Locate and identify every blood parasite.
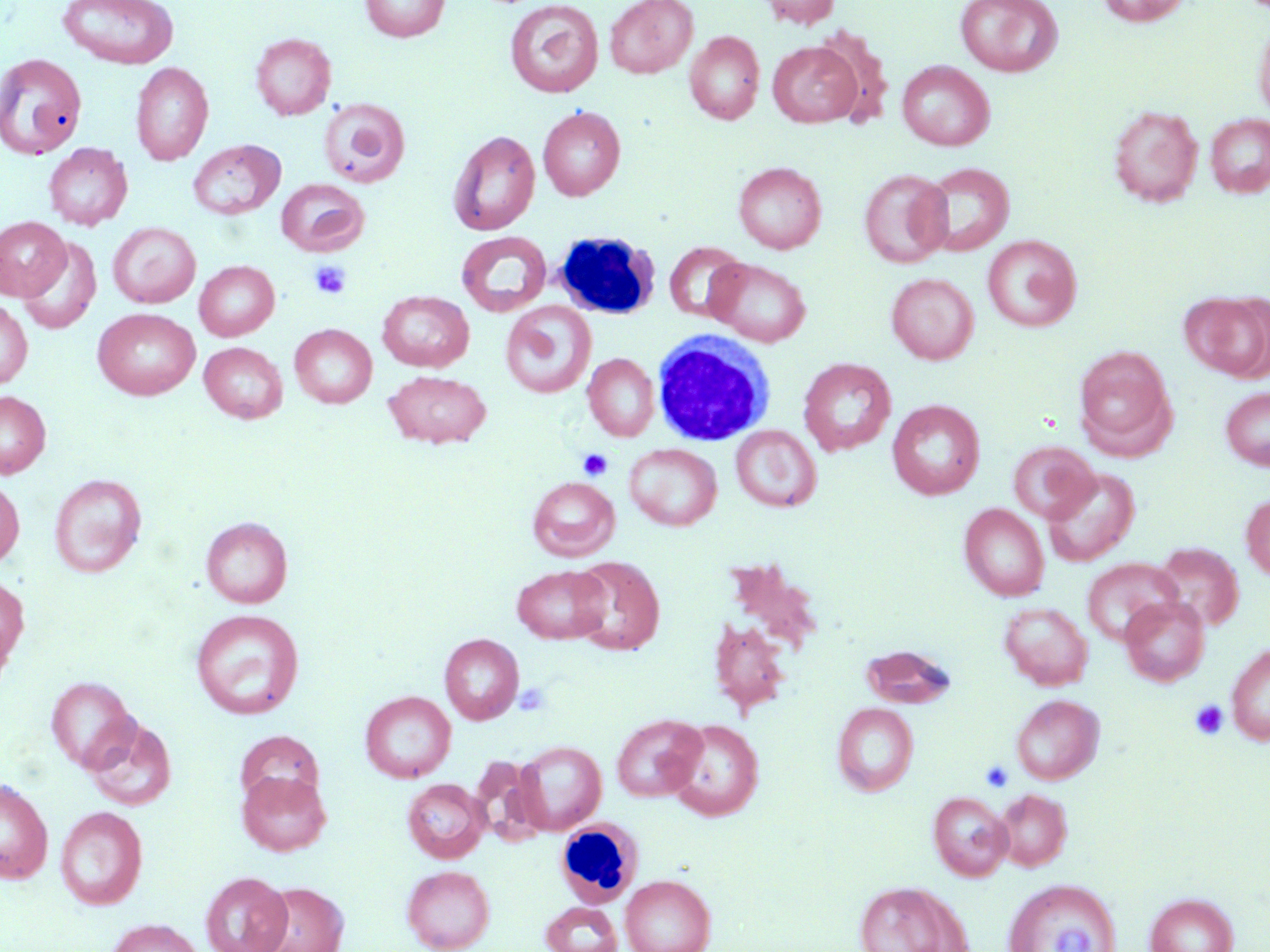

No blood parasites seen.

Approximate bounding boxes as (x1, y1, x2, y2) in pixels. Platelet locations: (309, 260, 352, 299), (578, 448, 612, 480), (513, 681, 551, 717), (1190, 699, 1228, 740), (981, 760, 1014, 792). Uninfected red blood cell locations: (57, 0, 179, 68), (360, 0, 450, 42), (604, 0, 698, 78), (758, 0, 842, 29), (955, 0, 1063, 77), (1097, 0, 1193, 27), (504, 1, 604, 98), (1253, 12, 1270, 122), (811, 26, 894, 125), (684, 31, 765, 125), (250, 32, 336, 120), (768, 41, 862, 127), (0, 52, 87, 160), (897, 60, 995, 151), (131, 62, 213, 165), (318, 98, 411, 188), (1108, 104, 1203, 207), (538, 106, 625, 200), (1205, 114, 1270, 198), (447, 130, 540, 236), (187, 139, 285, 220), (43, 143, 132, 230), (733, 161, 827, 254), (920, 162, 1014, 256), (859, 169, 952, 268), (276, 179, 369, 256), (0, 216, 70, 300), (108, 222, 201, 308), (456, 231, 552, 317), (982, 235, 1082, 332), (18, 237, 102, 335), (664, 241, 748, 323), (707, 258, 811, 346), (194, 260, 280, 341), (886, 272, 979, 364), (377, 290, 474, 372), (1186, 291, 1270, 383), (0, 299, 32, 389), (501, 301, 596, 399), (93, 308, 200, 400), (290, 324, 377, 408), (199, 342, 287, 423), (1073, 346, 1175, 454), (583, 354, 659, 440), (798, 358, 896, 456), (383, 370, 492, 449), (1220, 386, 1270, 471), (0, 390, 51, 478), (887, 400, 985, 499), (731, 425, 822, 512), (1008, 441, 1098, 522), (624, 443, 722, 530), (1041, 467, 1140, 567), (50, 473, 146, 578), (0, 476, 24, 569), (528, 476, 620, 561), (1241, 494, 1270, 582), (959, 503, 1049, 601), (201, 517, 293, 608), (1154, 543, 1243, 631), (569, 556, 664, 655), (723, 557, 824, 658), (1081, 558, 1182, 645), (512, 564, 610, 644), (0, 574, 29, 668), (1119, 596, 1209, 686), (999, 602, 1093, 690), (191, 609, 304, 719), (0, 612, 15, 699), (709, 618, 791, 715), (439, 633, 524, 724), (1226, 641, 1270, 746), (862, 644, 955, 708), (45, 675, 139, 773), (360, 691, 456, 783), (1012, 694, 1104, 784), (832, 703, 919, 796), (612, 714, 705, 802), (85, 717, 176, 811), (665, 719, 764, 821), (234, 730, 325, 808), (514, 740, 606, 834), (469, 755, 548, 845), (236, 770, 331, 856), (0, 776, 53, 884), (402, 779, 489, 863), (995, 788, 1072, 871), (928, 791, 1012, 881), (55, 806, 147, 910), (402, 865, 495, 952), (201, 872, 291, 952), (621, 874, 716, 952), (1003, 879, 1122, 952), (853, 880, 970, 952), (255, 882, 349, 952), (1145, 892, 1238, 952), (540, 902, 622, 952), (106, 918, 204, 952). White blood cell locations: (552, 231, 660, 320), (652, 328, 776, 446), (554, 809, 650, 909). Slide-level diagnosis: negative for blood parasites. May-Grünwald-Giemsa stain. One field of a larger specimen. Thin blood film. Image is 1270×952 pixels. 1000x magnification. Optical microscopy.